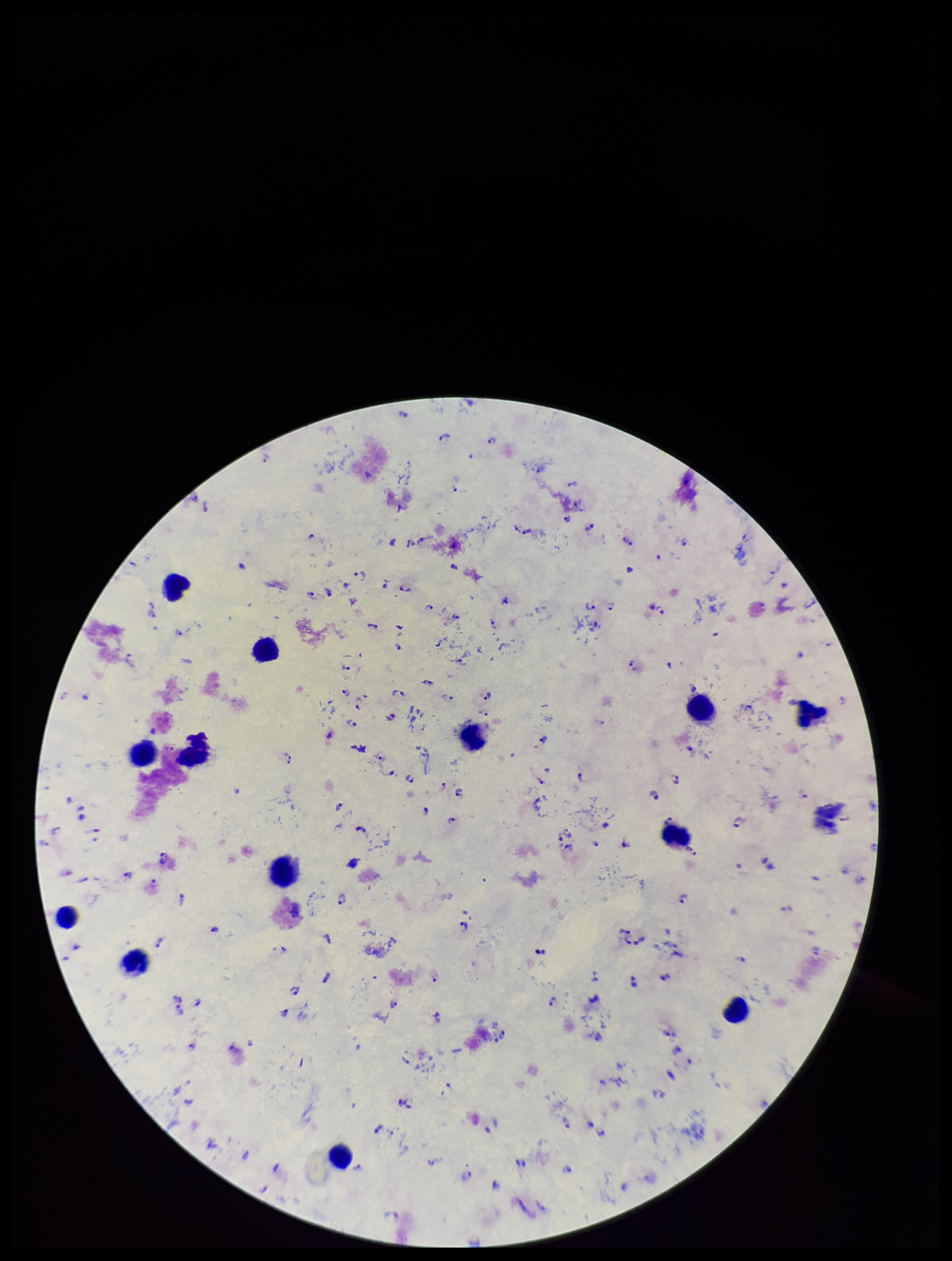
{
  "image_size": "952×1261 pixels",
  "parasite_count": 125,
  "capture": "smartphone photograph through the microscope eyepiece",
  "plasmodium_parasites": "identified",
  "species_reported_for_this_patient": "Plasmodium falciparum",
  "preparation": "thick",
  "field_of_view": "one from this slide",
  "stain": "Giemsa",
  "patient_malaria_status": "positive",
  "leukocyte_count": 13
}